Report the malaria status of this cell.
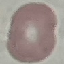
Uninfected.

Giemsa-stained preparation. Automatically extracted cell patch, resized to 64 × 64 pixels. Photographed with a smartphone camera at the microscope eyepiece. Thin blood film.